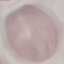 Malaria status: uninfected. Giemsa stain. Thin blood film. Photographed with a smartphone camera at the microscope eyepiece. Cell patch, automatically extracted from a larger field of view and resized to 64 × 64 pixels.